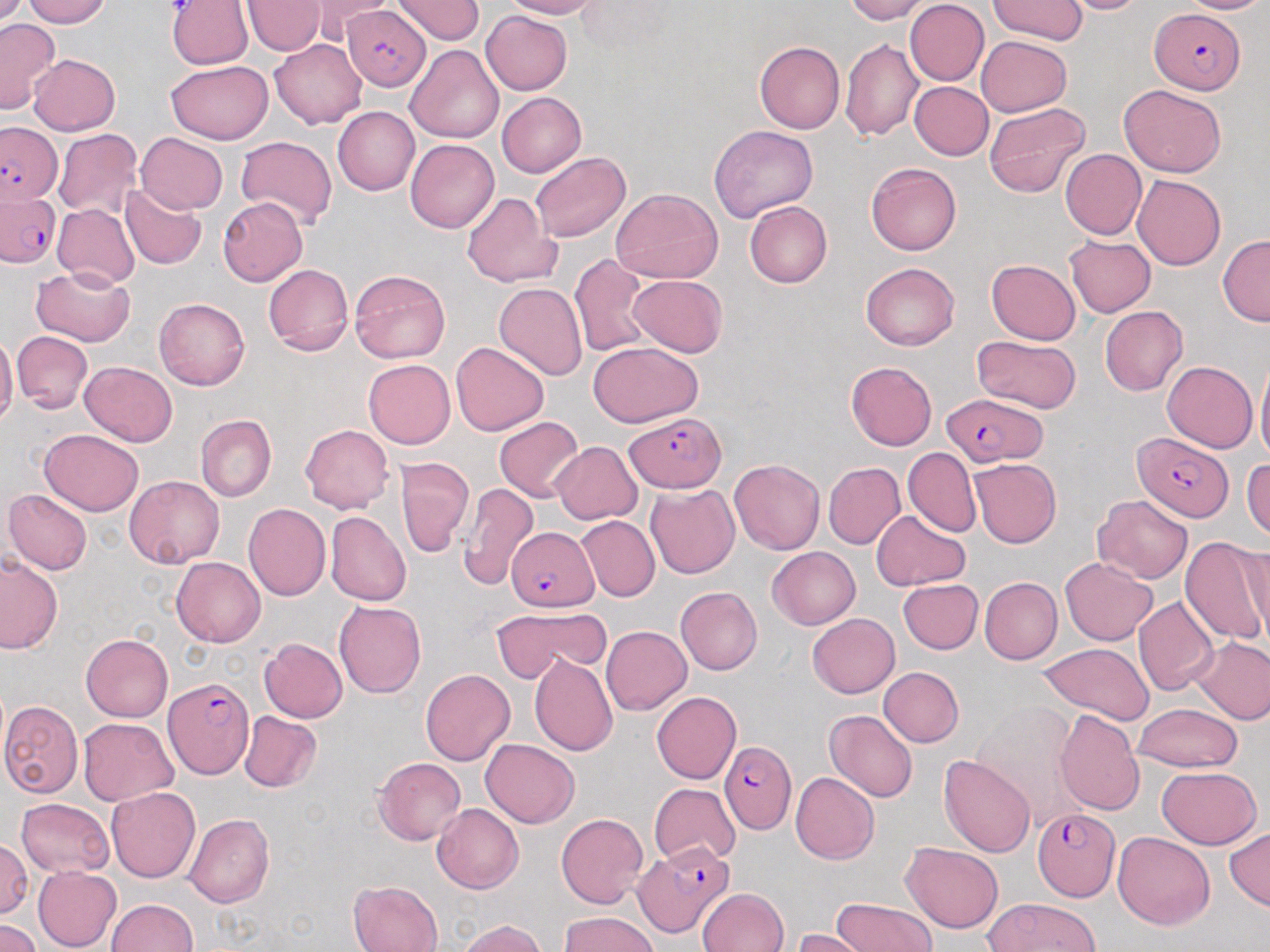

Approximate bounding boxes as named x1/y1/x2/y2 corners in pixels. Plasmodium falciparum-infected red blood cell locations: (x1=343, y1=4, x2=431, y2=91), (x1=1151, y1=8, x2=1247, y2=93), (x1=1, y1=122, x2=62, y2=207), (x1=0, y1=191, x2=60, y2=268), (x1=940, y1=393, x2=1048, y2=466), (x1=625, y1=411, x2=724, y2=491), (x1=1130, y1=434, x2=1234, y2=523), (x1=506, y1=527, x2=598, y2=611), (x1=164, y1=676, x2=252, y2=777), (x1=720, y1=741, x2=796, y2=833), (x1=1034, y1=809, x2=1122, y2=897), (x1=634, y1=842, x2=733, y2=939). Uninfected red blood cell locations: (x1=22, y1=0, x2=111, y2=28), (x1=304, y1=0, x2=396, y2=45), (x1=393, y1=0, x2=484, y2=45), (x1=497, y1=0, x2=601, y2=20), (x1=842, y1=0, x2=929, y2=23), (x1=990, y1=0, x2=1089, y2=44), (x1=1057, y1=0, x2=1151, y2=14), (x1=1178, y1=0, x2=1270, y2=14), (x1=241, y1=1, x2=325, y2=56), (x1=905, y1=1, x2=989, y2=85), (x1=167, y1=2, x2=253, y2=70), (x1=481, y1=10, x2=573, y2=95), (x1=0, y1=19, x2=60, y2=115), (x1=975, y1=36, x2=1070, y2=116), (x1=840, y1=38, x2=922, y2=141), (x1=270, y1=39, x2=366, y2=128), (x1=754, y1=41, x2=845, y2=134), (x1=405, y1=44, x2=504, y2=142), (x1=29, y1=54, x2=120, y2=134), (x1=165, y1=60, x2=273, y2=143), (x1=909, y1=82, x2=994, y2=160), (x1=1118, y1=83, x2=1227, y2=177), (x1=497, y1=92, x2=586, y2=178), (x1=983, y1=101, x2=1091, y2=198), (x1=333, y1=106, x2=419, y2=195), (x1=708, y1=124, x2=818, y2=222), (x1=53, y1=128, x2=143, y2=220), (x1=136, y1=132, x2=228, y2=213), (x1=234, y1=136, x2=336, y2=230), (x1=405, y1=139, x2=499, y2=233), (x1=1060, y1=149, x2=1146, y2=240), (x1=530, y1=151, x2=630, y2=243), (x1=866, y1=162, x2=962, y2=256), (x1=1133, y1=174, x2=1225, y2=270), (x1=119, y1=183, x2=206, y2=270), (x1=611, y1=187, x2=722, y2=284), (x1=462, y1=193, x2=560, y2=289), (x1=217, y1=198, x2=308, y2=285), (x1=744, y1=201, x2=832, y2=287), (x1=53, y1=204, x2=140, y2=288), (x1=1063, y1=236, x2=1156, y2=317), (x1=1217, y1=236, x2=1270, y2=326), (x1=569, y1=254, x2=650, y2=356), (x1=987, y1=259, x2=1080, y2=344), (x1=860, y1=262, x2=959, y2=350), (x1=263, y1=264, x2=352, y2=356), (x1=31, y1=266, x2=136, y2=346), (x1=349, y1=270, x2=451, y2=363), (x1=630, y1=275, x2=727, y2=356), (x1=494, y1=282, x2=587, y2=380), (x1=154, y1=298, x2=249, y2=391), (x1=1100, y1=305, x2=1186, y2=397), (x1=12, y1=330, x2=92, y2=414), (x1=0, y1=334, x2=18, y2=431), (x1=972, y1=335, x2=1080, y2=414), (x1=451, y1=342, x2=549, y2=435), (x1=588, y1=343, x2=703, y2=427), (x1=1255, y1=355, x2=1270, y2=465), (x1=363, y1=359, x2=455, y2=448), (x1=1163, y1=361, x2=1257, y2=452), (x1=80, y1=362, x2=177, y2=446), (x1=846, y1=362, x2=937, y2=450), (x1=195, y1=415, x2=277, y2=501), (x1=495, y1=416, x2=583, y2=501), (x1=300, y1=424, x2=394, y2=513), (x1=39, y1=429, x2=144, y2=516), (x1=552, y1=441, x2=643, y2=524), (x1=902, y1=447, x2=982, y2=538), (x1=396, y1=457, x2=474, y2=557), (x1=1243, y1=458, x2=1270, y2=541), (x1=969, y1=459, x2=1061, y2=548), (x1=729, y1=460, x2=824, y2=554), (x1=823, y1=462, x2=905, y2=549), (x1=125, y1=475, x2=223, y2=568), (x1=456, y1=481, x2=539, y2=590), (x1=646, y1=485, x2=739, y2=579), (x1=4, y1=490, x2=93, y2=575), (x1=1092, y1=494, x2=1192, y2=582), (x1=243, y1=503, x2=331, y2=600), (x1=325, y1=511, x2=412, y2=607), (x1=871, y1=511, x2=970, y2=591), (x1=577, y1=515, x2=659, y2=603), (x1=1178, y1=536, x2=1270, y2=646), (x1=1241, y1=541, x2=1269, y2=642), (x1=767, y1=546, x2=860, y2=629), (x1=0, y1=555, x2=63, y2=655), (x1=1059, y1=556, x2=1157, y2=645), (x1=172, y1=557, x2=266, y2=647), (x1=980, y1=577, x2=1062, y2=664), (x1=898, y1=578, x2=984, y2=654), (x1=675, y1=587, x2=762, y2=675), (x1=1133, y1=596, x2=1220, y2=696), (x1=334, y1=600, x2=426, y2=697), (x1=493, y1=606, x2=612, y2=680), (x1=806, y1=613, x2=900, y2=698), (x1=601, y1=625, x2=692, y2=715), (x1=81, y1=633, x2=172, y2=721), (x1=1192, y1=636, x2=1270, y2=724), (x1=260, y1=638, x2=347, y2=723), (x1=1040, y1=644, x2=1154, y2=724), (x1=529, y1=653, x2=618, y2=756), (x1=879, y1=667, x2=964, y2=747), (x1=421, y1=669, x2=516, y2=766), (x1=652, y1=690, x2=742, y2=784), (x1=1, y1=700, x2=83, y2=797), (x1=972, y1=700, x2=1084, y2=829), (x1=1133, y1=704, x2=1242, y2=772), (x1=1055, y1=709, x2=1143, y2=816), (x1=824, y1=710, x2=918, y2=803), (x1=239, y1=711, x2=322, y2=792), (x1=79, y1=719, x2=177, y2=804), (x1=481, y1=738, x2=579, y2=828), (x1=939, y1=754, x2=1035, y2=858), (x1=372, y1=756, x2=465, y2=845), (x1=1157, y1=765, x2=1262, y2=848), (x1=790, y1=772, x2=879, y2=864), (x1=648, y1=784, x2=740, y2=866), (x1=107, y1=787, x2=200, y2=882), (x1=16, y1=797, x2=112, y2=877), (x1=432, y1=803, x2=524, y2=893), (x1=556, y1=812, x2=649, y2=908), (x1=184, y1=814, x2=273, y2=909), (x1=1225, y1=827, x2=1270, y2=910), (x1=1112, y1=831, x2=1216, y2=930), (x1=0, y1=836, x2=32, y2=918), (x1=900, y1=842, x2=1003, y2=932), (x1=32, y1=866, x2=122, y2=952), (x1=348, y1=880, x2=442, y2=952), (x1=698, y1=888, x2=789, y2=952), (x1=832, y1=897, x2=935, y2=952), (x1=983, y1=897, x2=1100, y2=952), (x1=107, y1=899, x2=198, y2=952), (x1=559, y1=912, x2=660, y2=952), (x1=0, y1=918, x2=42, y2=952), (x1=460, y1=919, x2=549, y2=952), (x1=793, y1=928, x2=874, y2=952). Slide-level diagnosis: Plasmodium falciparum. One field of a larger specimen. Image is 1270×952 pixels. Optical microscopy. 1000x magnification. Thin blood film. May-Grünwald-Giemsa-stained preparation.